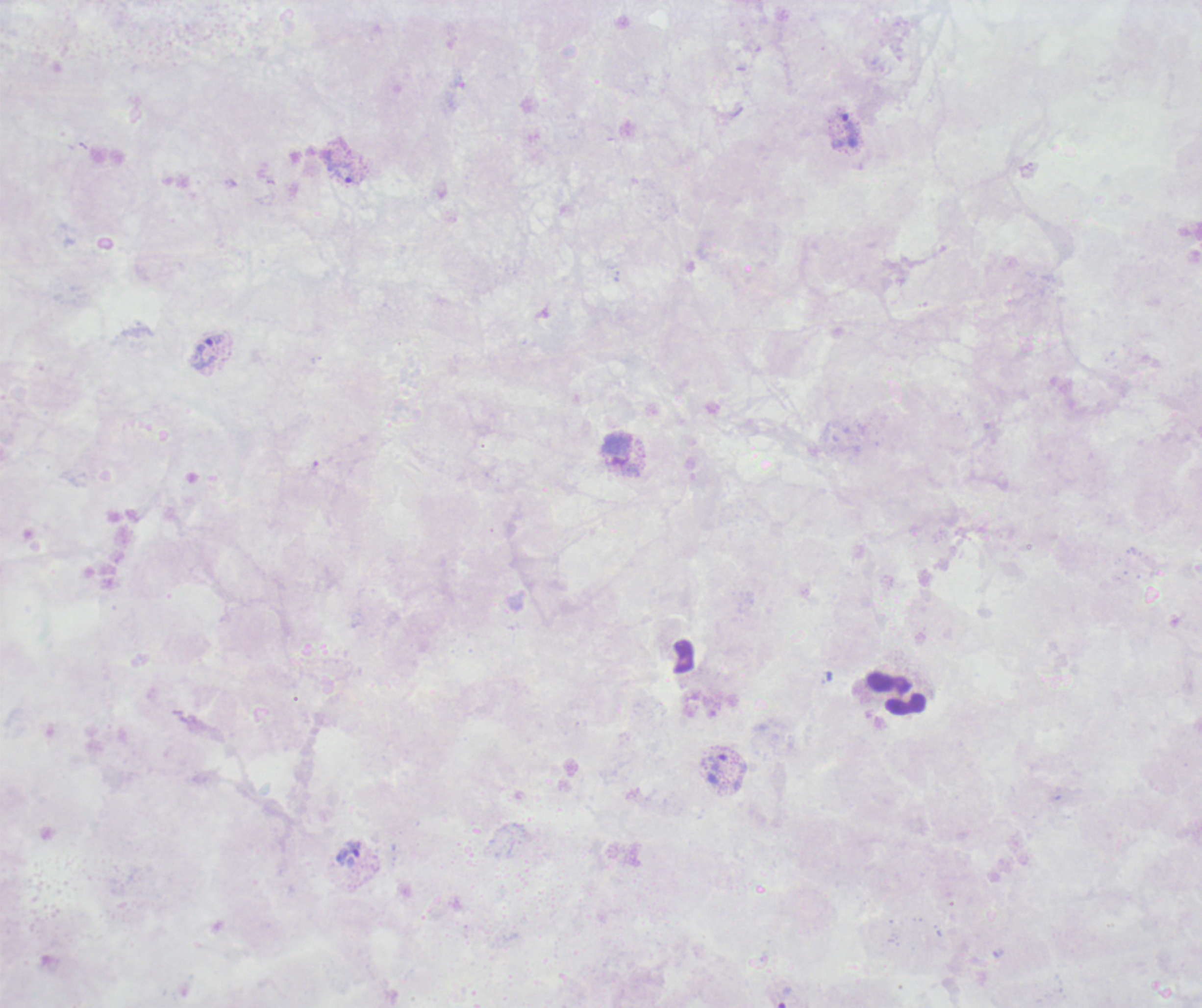
Approximate object centers, in pixels from the top-left corner.
Summary:
  - Leukocyte locations: (x=896, y=693)
  - Trophozoite locations: (x=848, y=122), (x=341, y=172), (x=207, y=352), (x=719, y=762), (x=354, y=849), (x=783, y=996)
  - Magnification: 100x
  - Field of view: single
  - Result: Plasmodium parasites identified
  - Image size: 1202×1008 pixels
  - Stain: Romanowsky
  - Context: previously used in a real diagnosis
  - Coloration quality: bad
  - Preparation: thick smear of blood
  - Background quality: poor